Give the preparation type.
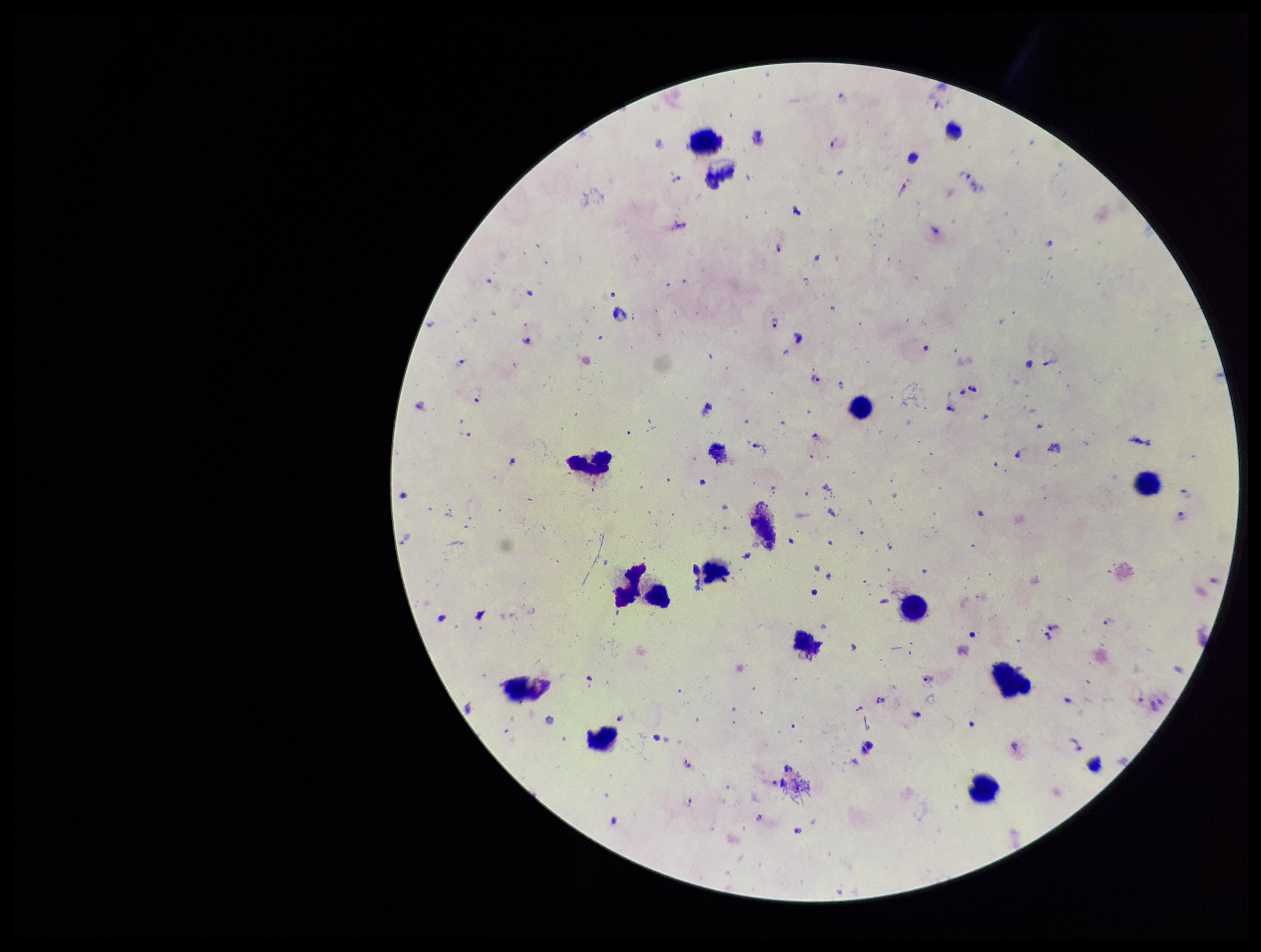
A thick smear.

Species reported for this patient: Plasmodium falciparum. Smartphone photograph taken through the eyepiece of a microscope. Plasmodium parasites: detected. Patient malaria status: infected. Stained with Giemsa. One field from this slide. Leukocyte count: 15. Parasite count: 42. Image is 1261×952 pixels.